Give the position of every Plasmodium parasite.
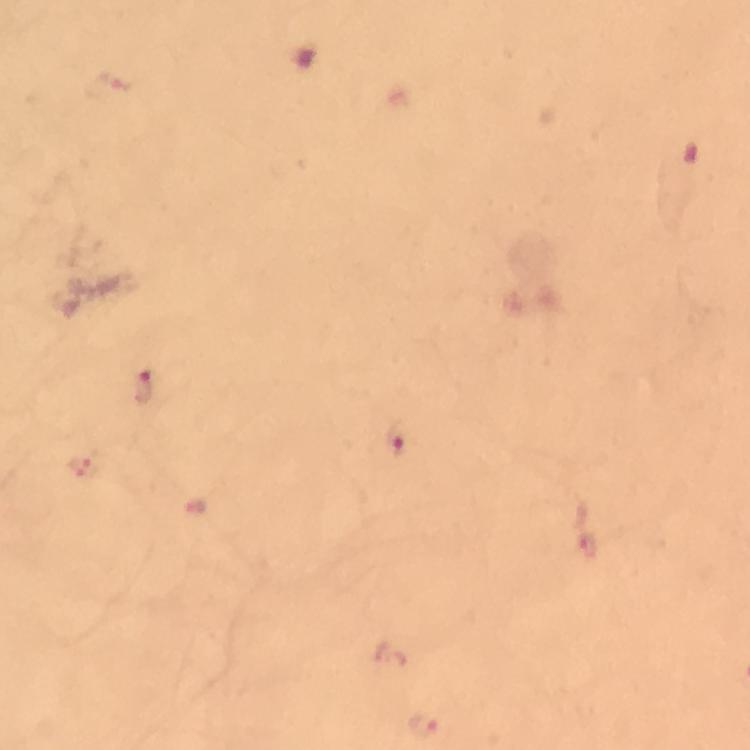
Approximate centers as (x, y) in pixels.
Plasmodium parasites: (142, 388), (398, 438), (80, 468), (589, 544), (423, 727).

stain: Giemsa
context: from a malaria diagnostic workup
preparation: thick blood film
cropped_from: a single field of view
immersion_oil: used
image_size: 750×750 pixels
capture: smartphone photograph through a microscope
magnification: 100x